Report the malaria status of this cell.
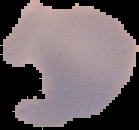

Uninfected.

Summary:
  - Preparation: thin blood smear
  - Image size: 139×130 pixels
  - Image type: segmented cell region with the area outside set to black